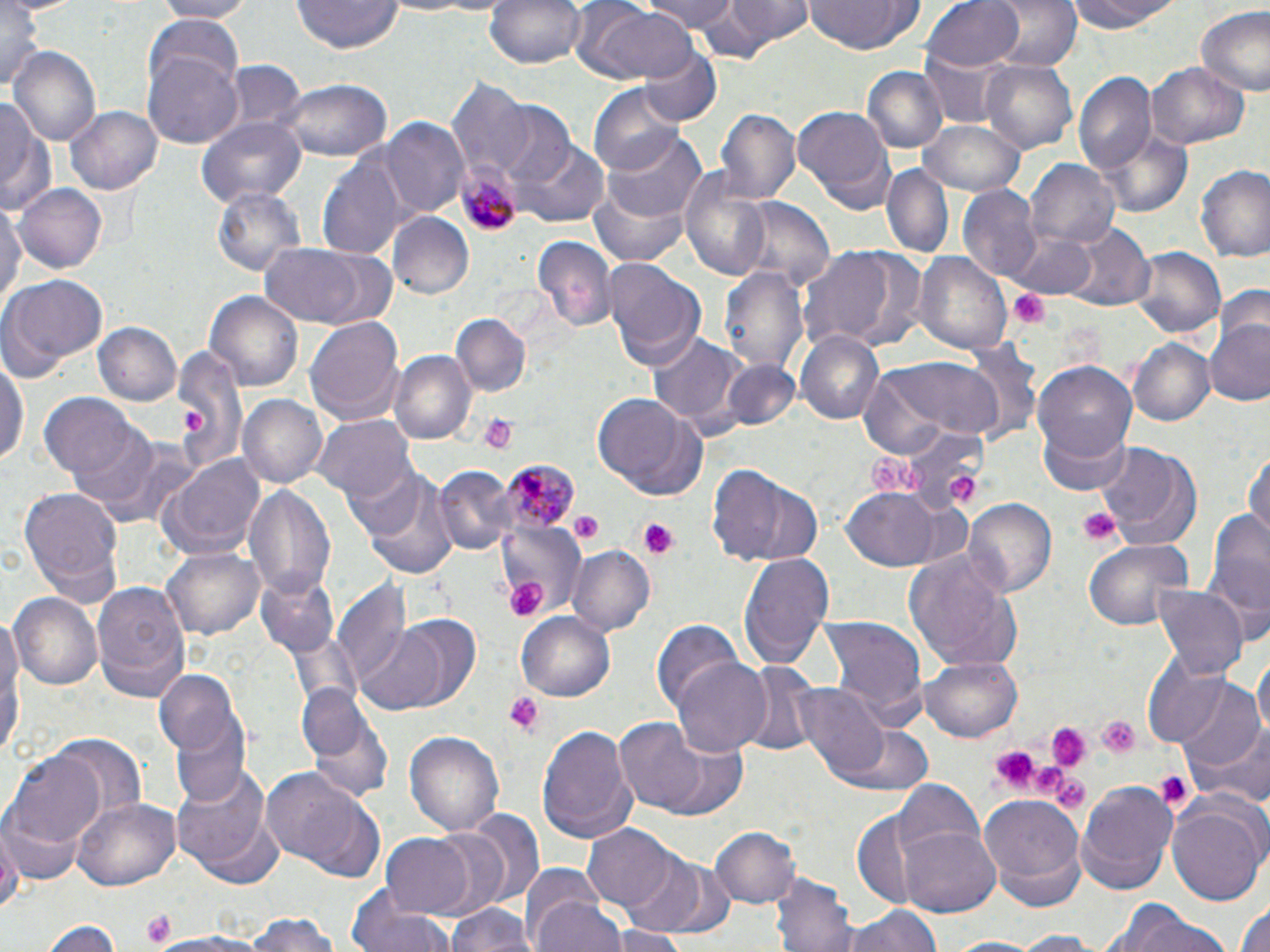

Summary:
  - Coordinate format: approximate bounding boxes as [x1, y1, x2, y2] in pixels
  - Plasmodium malariae-infected red blood cell locations: [454, 155, 522, 237], [501, 457, 576, 534]
  - Uninfected red blood cell locations: [150, 0, 254, 21], [484, 0, 585, 72], [567, 0, 691, 85], [644, 0, 743, 38], [719, 0, 815, 52], [923, 0, 1025, 73], [989, 0, 1081, 74], [1068, 0, 1186, 34], [293, 1, 400, 53], [802, 1, 923, 56], [0, 3, 50, 96], [1194, 5, 1270, 96], [148, 17, 244, 96], [9, 45, 101, 148], [637, 45, 720, 127], [145, 53, 242, 149], [981, 60, 1078, 154], [226, 62, 305, 135], [1147, 62, 1249, 151], [861, 66, 945, 153], [1074, 73, 1157, 173], [446, 78, 532, 181], [279, 79, 392, 160], [591, 89, 686, 174], [0, 94, 50, 215], [490, 103, 579, 192], [67, 106, 162, 193], [792, 107, 896, 213], [715, 108, 799, 207], [196, 116, 306, 209], [378, 118, 470, 219], [920, 119, 1026, 197], [1092, 122, 1197, 219], [606, 130, 706, 227], [515, 142, 610, 228], [317, 153, 410, 258], [1026, 159, 1120, 249], [880, 164, 951, 258], [677, 166, 771, 281], [1195, 166, 1270, 264], [14, 182, 109, 273], [586, 184, 696, 267], [213, 186, 304, 279], [959, 188, 1042, 282], [734, 198, 832, 291], [0, 199, 25, 315], [389, 212, 474, 298], [1058, 222, 1154, 313], [1006, 229, 1101, 299], [530, 234, 616, 333], [259, 243, 393, 330], [803, 244, 915, 351], [1132, 248, 1226, 346], [913, 251, 1013, 354], [601, 258, 707, 368], [720, 264, 809, 377], [0, 273, 109, 381], [203, 290, 306, 391], [305, 315, 404, 427], [452, 315, 531, 399], [1206, 315, 1270, 408], [92, 323, 182, 407], [797, 331, 885, 425], [648, 332, 740, 428], [1128, 340, 1214, 425], [170, 349, 246, 469], [390, 350, 477, 443], [1, 354, 27, 474], [859, 356, 1013, 453], [714, 359, 804, 433], [1032, 361, 1137, 468], [39, 394, 142, 481], [590, 394, 709, 502], [236, 395, 326, 489], [1035, 415, 1136, 498], [316, 416, 414, 503], [78, 434, 198, 531], [1093, 440, 1201, 546], [1246, 449, 1270, 539], [154, 453, 267, 563], [705, 464, 812, 568], [431, 466, 514, 557], [354, 469, 458, 580], [244, 481, 337, 601], [840, 483, 947, 570], [17, 486, 124, 601], [963, 499, 1057, 602], [1203, 504, 1270, 631], [1083, 538, 1195, 631], [566, 545, 655, 638], [162, 546, 265, 640], [739, 550, 835, 668], [903, 551, 1020, 672], [255, 572, 339, 657], [92, 581, 191, 699], [331, 582, 413, 685], [1152, 584, 1247, 680], [9, 593, 102, 692], [359, 611, 485, 715], [517, 611, 616, 702], [818, 614, 928, 722], [652, 619, 751, 715], [1253, 652, 1270, 744], [920, 657, 1024, 742], [671, 658, 773, 758], [738, 661, 822, 758], [154, 669, 244, 757], [1168, 676, 1266, 776], [790, 681, 894, 780], [296, 684, 371, 763], [300, 692, 395, 803], [172, 719, 251, 805], [614, 719, 708, 812], [829, 722, 937, 797], [536, 724, 637, 844], [1189, 726, 1270, 811], [404, 730, 504, 836], [50, 735, 148, 830], [640, 735, 750, 822], [8, 751, 106, 848], [169, 760, 276, 881], [261, 769, 379, 874], [894, 778, 986, 866], [1076, 781, 1178, 890], [979, 794, 1084, 898], [72, 798, 182, 891], [1168, 801, 1264, 907], [1, 808, 83, 886], [461, 809, 546, 914], [0, 817, 21, 918], [581, 825, 677, 913], [710, 826, 801, 910], [901, 826, 999, 915], [380, 833, 476, 918], [621, 853, 716, 936], [519, 862, 606, 943], [774, 874, 856, 952], [348, 888, 452, 952], [532, 896, 628, 952], [1234, 899, 1270, 952], [446, 902, 537, 952], [839, 905, 944, 952], [1119, 908, 1239, 952], [240, 914, 349, 952], [43, 919, 121, 952], [608, 925, 689, 952], [1001, 930, 1107, 950], [147, 932, 277, 952], [937, 936, 1054, 952]
  - Platelet locations: [1005, 287, 1053, 329], [181, 409, 204, 432], [478, 414, 518, 454], [867, 451, 932, 495], [947, 474, 981, 503], [1079, 507, 1121, 548], [568, 511, 604, 543], [636, 517, 682, 560], [504, 575, 548, 625], [503, 693, 545, 735], [1096, 715, 1140, 760], [1045, 721, 1092, 772], [987, 742, 1042, 794], [1155, 770, 1191, 811], [1054, 774, 1088, 811], [141, 910, 178, 948]
  - Slide-level diagnosis: Plasmodium malariae
  - Stain: May-Grünwald-Giemsa
  - Magnification: 1000x
  - Modality: light microscopy
  - Image size: 1270×952 pixels
  - Preparation: thin blood film
  - Field of view: one of a larger specimen